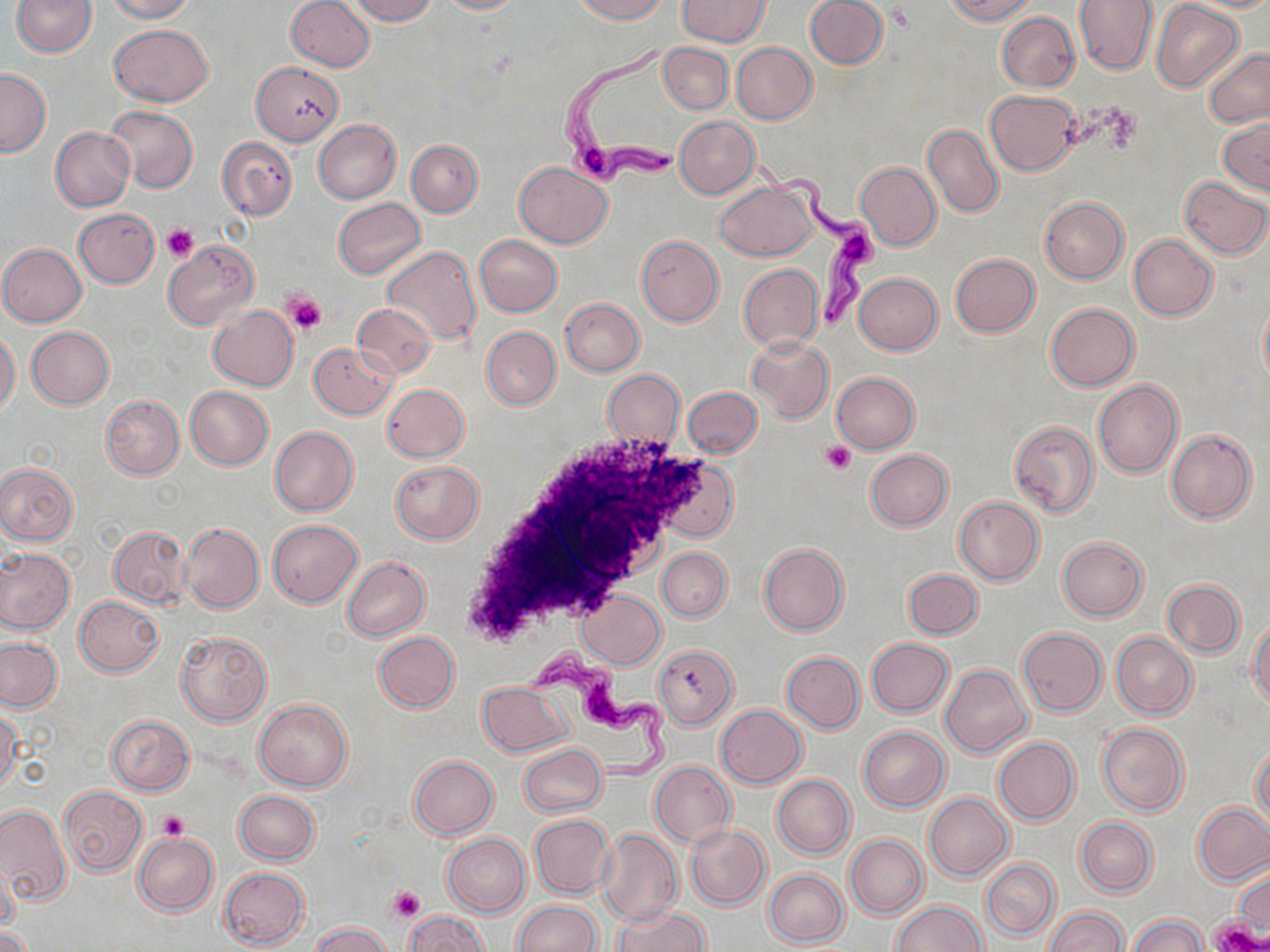 Approximate bounding boxes as named x1/y1/x2/y2 corners in pixels. Platelet locations: (x1=161, y1=224, x2=198, y2=264), (x1=284, y1=291, x2=326, y2=335), (x1=822, y1=439, x2=856, y2=474), (x1=158, y1=811, x2=188, y2=841), (x1=388, y1=886, x2=425, y2=922), (x1=1211, y1=917, x2=1262, y2=951). Trypanosoma brucei locations: (x1=558, y1=38, x2=689, y2=188), (x1=751, y1=154, x2=878, y2=331), (x1=524, y1=645, x2=675, y2=789). Uninfected red blood cell locations: (x1=106, y1=0, x2=195, y2=22), (x1=286, y1=0, x2=375, y2=72), (x1=346, y1=0, x2=436, y2=24), (x1=435, y1=0, x2=525, y2=14), (x1=574, y1=0, x2=666, y2=23), (x1=677, y1=0, x2=770, y2=47), (x1=804, y1=0, x2=887, y2=69), (x1=945, y1=0, x2=1036, y2=23), (x1=1075, y1=0, x2=1158, y2=75), (x1=10, y1=1, x2=96, y2=57), (x1=1152, y1=1, x2=1244, y2=91), (x1=995, y1=11, x2=1079, y2=91), (x1=110, y1=23, x2=213, y2=106), (x1=732, y1=42, x2=816, y2=124), (x1=658, y1=43, x2=732, y2=114), (x1=1202, y1=48, x2=1270, y2=127), (x1=252, y1=61, x2=344, y2=145), (x1=0, y1=68, x2=51, y2=157), (x1=986, y1=90, x2=1079, y2=174), (x1=106, y1=105, x2=198, y2=193), (x1=676, y1=117, x2=760, y2=197), (x1=314, y1=119, x2=401, y2=202), (x1=1219, y1=119, x2=1269, y2=194), (x1=922, y1=123, x2=1003, y2=218), (x1=51, y1=128, x2=134, y2=212), (x1=218, y1=137, x2=296, y2=219), (x1=407, y1=140, x2=483, y2=217), (x1=514, y1=161, x2=611, y2=247), (x1=856, y1=161, x2=941, y2=251), (x1=1180, y1=176, x2=1270, y2=259), (x1=715, y1=180, x2=819, y2=261), (x1=1040, y1=197, x2=1128, y2=283), (x1=334, y1=198, x2=425, y2=277), (x1=73, y1=209, x2=160, y2=287), (x1=1129, y1=234, x2=1218, y2=321), (x1=473, y1=235, x2=563, y2=316), (x1=636, y1=235, x2=723, y2=326), (x1=164, y1=241, x2=258, y2=328), (x1=0, y1=244, x2=86, y2=326), (x1=382, y1=245, x2=482, y2=347), (x1=950, y1=254, x2=1040, y2=337), (x1=740, y1=263, x2=824, y2=351), (x1=853, y1=273, x2=943, y2=354), (x1=560, y1=298, x2=644, y2=376), (x1=1259, y1=300, x2=1270, y2=390), (x1=353, y1=303, x2=435, y2=378), (x1=209, y1=304, x2=299, y2=390), (x1=1046, y1=304, x2=1139, y2=391), (x1=26, y1=326, x2=114, y2=408), (x1=482, y1=326, x2=561, y2=409), (x1=0, y1=332, x2=20, y2=415), (x1=747, y1=336, x2=833, y2=422), (x1=309, y1=342, x2=397, y2=419), (x1=602, y1=370, x2=685, y2=447), (x1=832, y1=372, x2=921, y2=453), (x1=1093, y1=379, x2=1183, y2=478), (x1=381, y1=384, x2=469, y2=462), (x1=185, y1=385, x2=272, y2=470), (x1=683, y1=387, x2=762, y2=458), (x1=101, y1=396, x2=184, y2=479), (x1=1009, y1=420, x2=1100, y2=517), (x1=269, y1=427, x2=358, y2=516), (x1=1166, y1=430, x2=1256, y2=523), (x1=865, y1=450, x2=953, y2=530), (x1=655, y1=456, x2=738, y2=542), (x1=389, y1=461, x2=484, y2=543), (x1=0, y1=463, x2=77, y2=545), (x1=955, y1=496, x2=1044, y2=584), (x1=268, y1=520, x2=362, y2=607), (x1=180, y1=523, x2=264, y2=614), (x1=107, y1=527, x2=189, y2=609), (x1=1057, y1=537, x2=1148, y2=621), (x1=759, y1=542, x2=849, y2=635), (x1=0, y1=547, x2=75, y2=634), (x1=658, y1=547, x2=732, y2=622), (x1=342, y1=557, x2=431, y2=641), (x1=903, y1=568, x2=983, y2=638), (x1=1164, y1=579, x2=1245, y2=657), (x1=576, y1=587, x2=666, y2=670), (x1=75, y1=596, x2=165, y2=675), (x1=1249, y1=621, x2=1270, y2=708), (x1=1018, y1=627, x2=1107, y2=716), (x1=175, y1=631, x2=272, y2=725), (x1=373, y1=631, x2=460, y2=713), (x1=1112, y1=632, x2=1197, y2=719), (x1=0, y1=638, x2=62, y2=712), (x1=866, y1=638, x2=953, y2=717), (x1=653, y1=644, x2=738, y2=730), (x1=781, y1=651, x2=864, y2=734), (x1=942, y1=664, x2=1033, y2=757), (x1=478, y1=682, x2=572, y2=756), (x1=254, y1=699, x2=352, y2=791), (x1=716, y1=705, x2=806, y2=787), (x1=0, y1=708, x2=21, y2=794), (x1=105, y1=715, x2=194, y2=795), (x1=1097, y1=722, x2=1189, y2=816), (x1=858, y1=725, x2=949, y2=811), (x1=993, y1=737, x2=1080, y2=826), (x1=520, y1=744, x2=607, y2=816), (x1=1252, y1=746, x2=1270, y2=829), (x1=408, y1=756, x2=499, y2=838), (x1=649, y1=760, x2=735, y2=847), (x1=773, y1=775, x2=855, y2=858), (x1=58, y1=785, x2=146, y2=876), (x1=233, y1=790, x2=321, y2=865), (x1=924, y1=792, x2=1013, y2=881), (x1=0, y1=803, x2=70, y2=907), (x1=1194, y1=803, x2=1270, y2=886), (x1=529, y1=814, x2=612, y2=899), (x1=1076, y1=817, x2=1156, y2=896), (x1=686, y1=824, x2=770, y2=910), (x1=596, y1=828, x2=682, y2=926), (x1=134, y1=833, x2=218, y2=915), (x1=441, y1=833, x2=530, y2=916), (x1=845, y1=834, x2=926, y2=919), (x1=981, y1=859, x2=1059, y2=940), (x1=0, y1=861, x2=20, y2=939), (x1=218, y1=867, x2=309, y2=949), (x1=1233, y1=867, x2=1270, y2=935), (x1=764, y1=869, x2=848, y2=947), (x1=512, y1=901, x2=602, y2=952), (x1=890, y1=901, x2=987, y2=952), (x1=614, y1=906, x2=709, y2=952), (x1=1044, y1=906, x2=1129, y2=951), (x1=405, y1=911, x2=487, y2=952), (x1=1131, y1=915, x2=1207, y2=952), (x1=309, y1=922, x2=392, y2=952), (x1=0, y1=926, x2=32, y2=952). Slide-level diagnosis: Trypanosoma brucei. 1000x magnification. One field of a larger specimen. May-Grünwald-Giemsa stain. Light microscopy. Thin blood smear. Image is 1270×952 pixels.